Identify the cell.
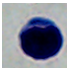

This is a leukocyte.

Captured at 1000x magnification. Photomicrograph.